Point out each malaria parasite.
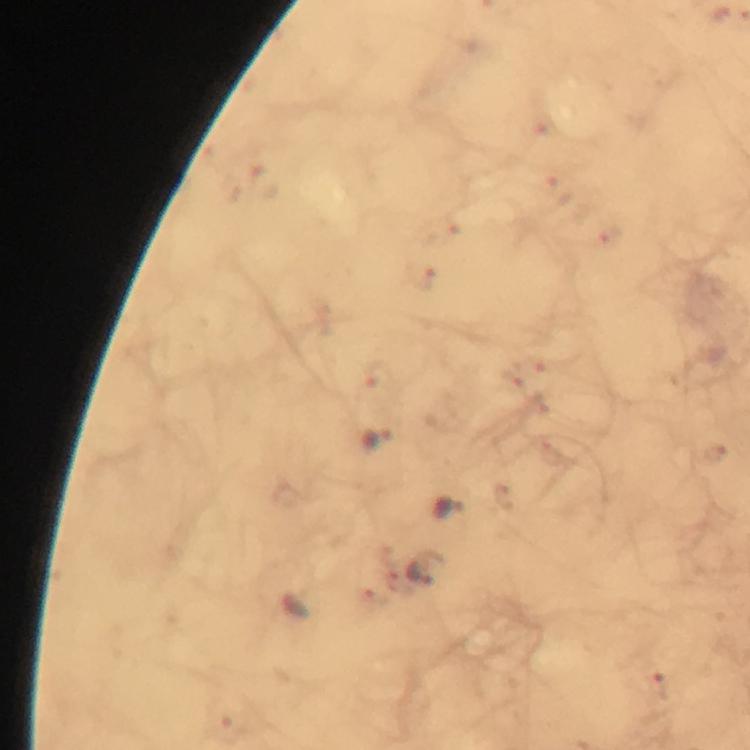

Approximate centers as [x, y] in pixels.
Malaria parasites: [261, 181], [556, 190], [607, 238], [419, 275], [378, 373], [377, 439], [716, 452], [451, 508], [425, 573], [297, 608], [660, 687], [228, 730].

cropped from = one field of view
magnification = 100x
context = from a diagnostic examination for malaria
stain = Giemsa
preparation = thick blood film
immersion oil = used
capture = smartphone photograph through a microscope
image size = 750×750 pixels